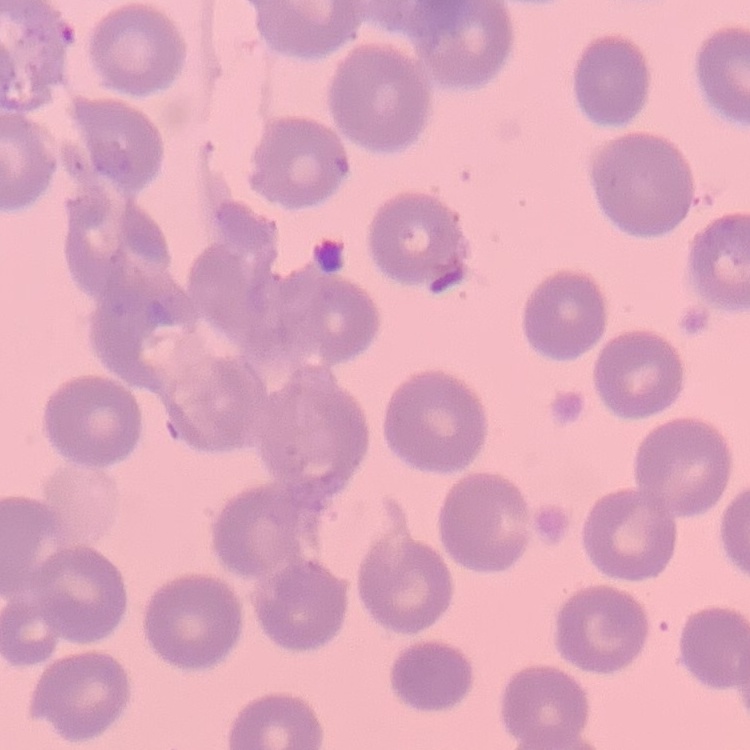
Summary:
  - Red blood cell morphology: no rouleaux formation
  - Preparation: thin peripheral smear
  - Stain: Field's or Giemsa
  - Image type: square crop of a larger photomicrograph